Evaluate for Plasmodium parasites.
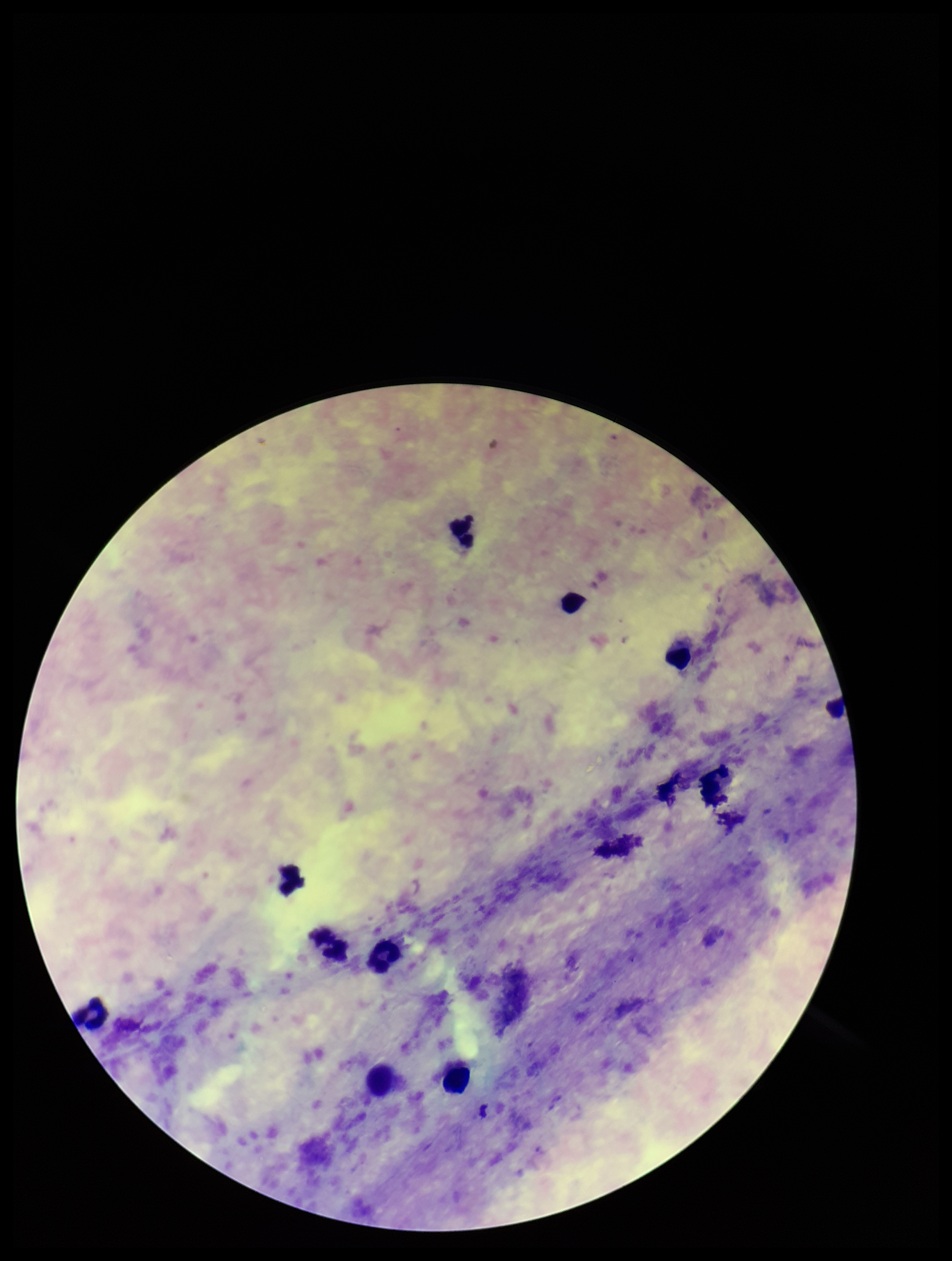
None seen.

Leukocyte count: 11. Parasite count: 0. Single field of view. Species reported for this patient: Plasmodium falciparum. Patient malaria status: infected. Image is 952×1261 pixels. Preparation: thick. Smartphone photograph taken through the eyepiece of a microscope. Stained with Giemsa.